Assess this cell for malaria.
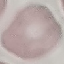

Uninfected.

Summary:
  - Stain: Giemsa
  - Preparation: thin blood film
  - Image type: automatically extracted cell patch, resized to 64 × 64 pixels
  - Capture: smartphone camera at the microscope eyepiece